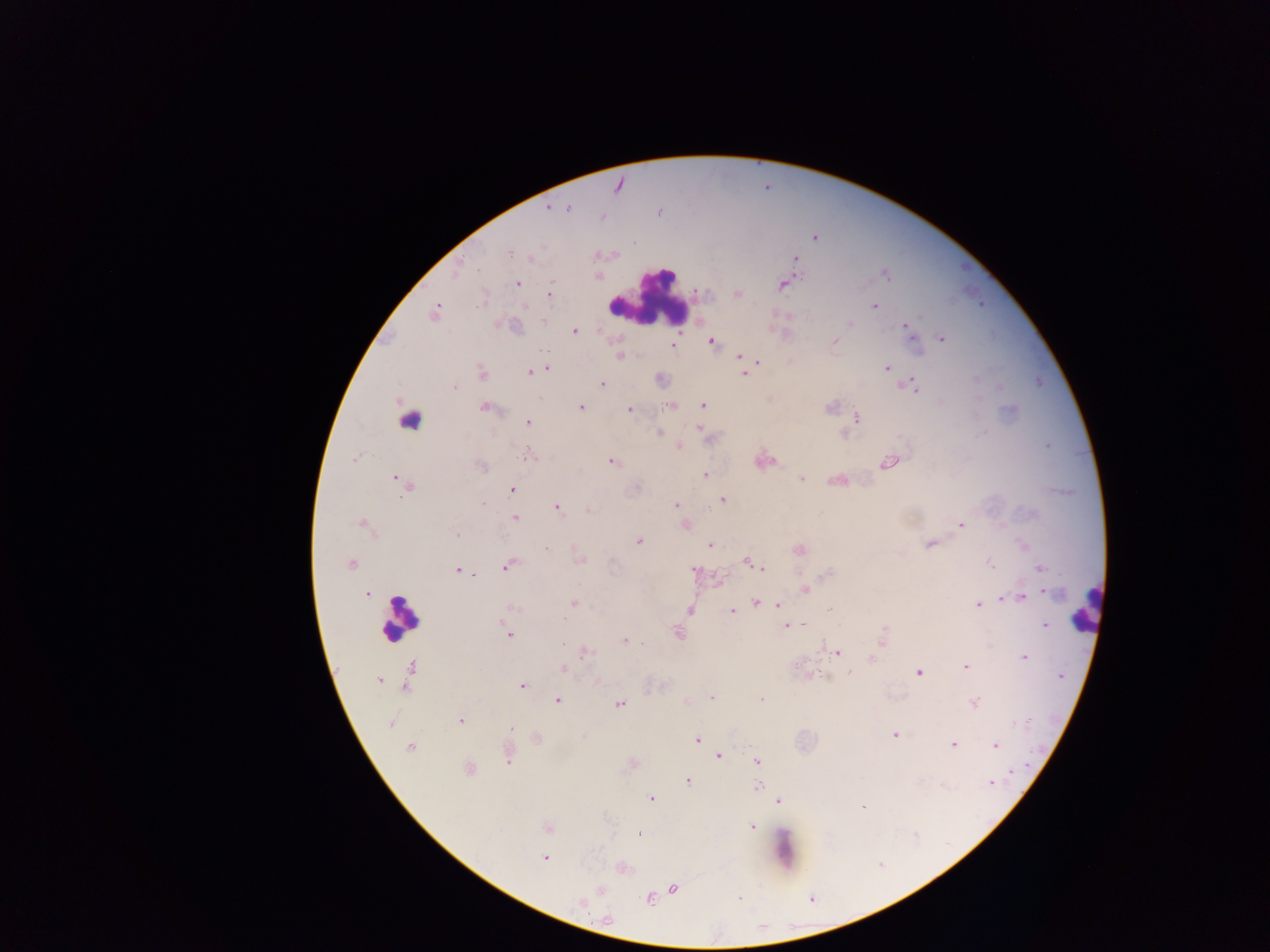

Approximate centers as [x, y] in pixels. Plasmodium parasite locations: [618, 186], [548, 207], [567, 207], [659, 211], [602, 216], [634, 242], [509, 253], [531, 258], [796, 260], [886, 274], [517, 283], [783, 285], [549, 293], [737, 294], [874, 307], [435, 312], [544, 321], [850, 324], [907, 328], [575, 332], [942, 339], [835, 341], [712, 342], [673, 346], [620, 356], [740, 356], [758, 362], [888, 367], [546, 369], [530, 372], [481, 373], [744, 374], [602, 383], [913, 386], [454, 387], [540, 398], [702, 405], [672, 406], [581, 407], [830, 407], [485, 408], [629, 409], [856, 418], [528, 422], [701, 429], [659, 433], [680, 446], [1047, 446], [528, 455], [354, 459], [611, 461], [889, 463], [481, 466], [705, 475], [802, 478], [396, 479], [512, 489], [722, 499], [483, 505], [676, 506], [557, 508], [588, 511], [514, 517], [360, 524], [961, 525], [686, 526], [456, 535], [639, 540], [930, 544], [710, 546], [546, 548], [799, 549], [579, 561], [747, 562], [989, 562], [351, 564], [508, 565], [762, 568], [1040, 568], [457, 570], [695, 570], [827, 574], [474, 575], [806, 590], [366, 594], [1051, 594], [1023, 596], [1003, 599], [574, 603], [756, 603], [777, 604], [977, 604], [514, 608], [830, 609], [690, 610], [731, 611], [787, 625], [803, 625], [1045, 625], [884, 627], [678, 633], [509, 636], [624, 641], [882, 642], [641, 643], [563, 644], [587, 652], [837, 652], [1023, 657], [872, 659], [966, 667], [563, 669], [812, 673], [849, 673], [919, 673], [379, 681], [522, 686], [711, 698], [761, 699], [558, 700], [974, 703], [619, 704], [461, 721], [1027, 721], [390, 723], [511, 727], [894, 735], [536, 738], [697, 739], [953, 744], [995, 745], [410, 748], [719, 756], [508, 761], [757, 761], [469, 768], [1011, 772], [687, 781], [990, 784], [758, 785], [943, 785], [652, 799], [778, 801], [863, 808], [752, 827], [546, 828], [638, 834], [544, 858], [673, 888], [601, 890], [740, 897], [649, 900], [581, 903], [608, 920]. Leukocyte locations: [645, 297], [417, 419], [1085, 608], [399, 618]. Image is 1270×952 pixels. One field of view. Thick blood smear. Collected in Ghana. Photographed through a microscope with a mobile-phone camera.